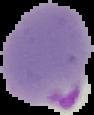

Summary:
  - Image size: 94×115 pixels
  - Preparation: thin blood film
  - Image type: segmented cell region with the area outside set to black
  - Malaria status: parasitized